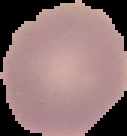
preparation: thin blood smear
malaria_status: uninfected
image_type: cell region segmented out of the field of view; surrounding area masked to black
image_size: 127×136 pixels